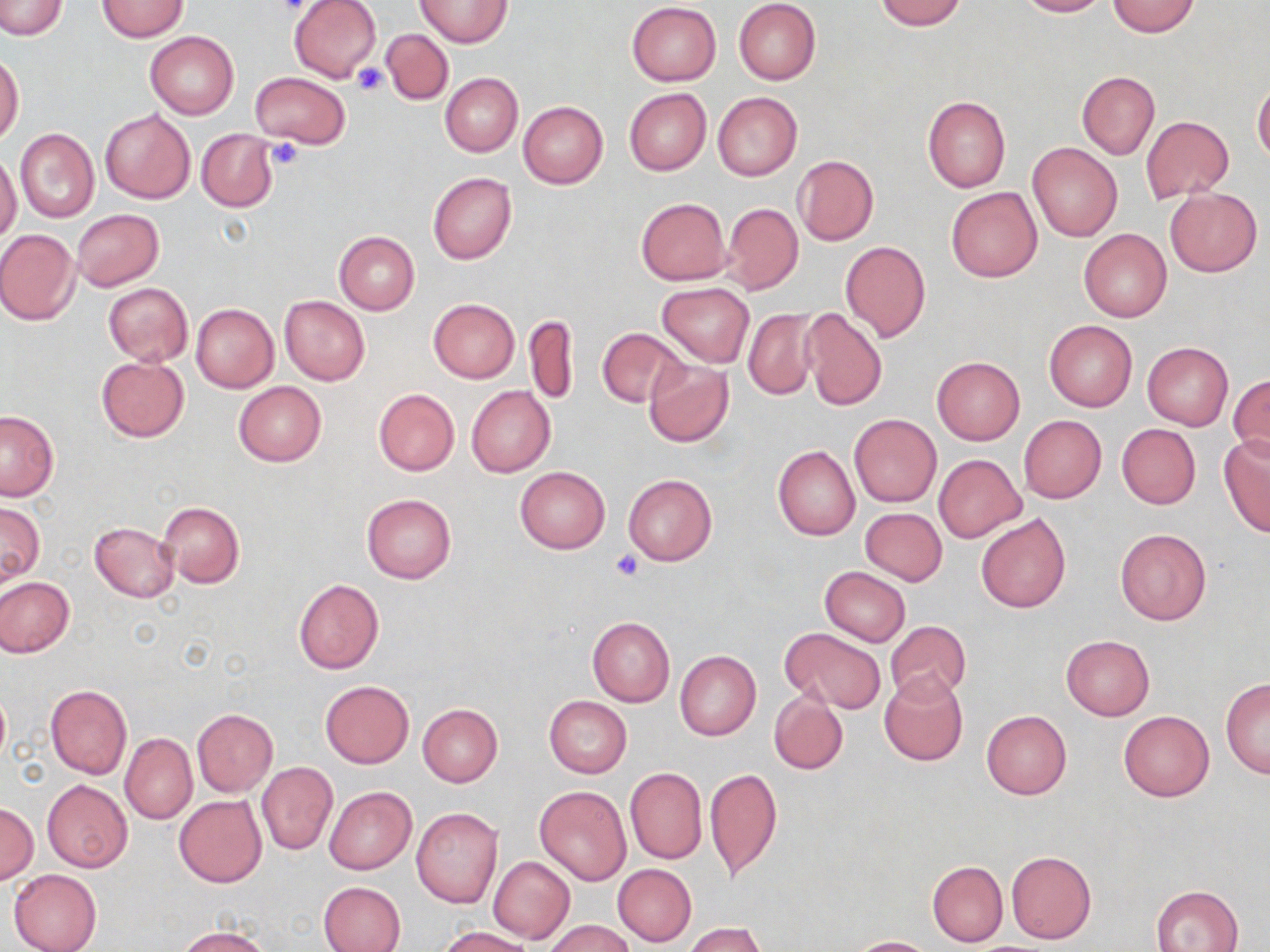

Approximate bounding boxes as named x1/y1/x2/y2 corners in pixels. Uninfected red blood cell locations: (x1=0, y1=0, x2=66, y2=40), (x1=289, y1=0, x2=380, y2=84), (x1=875, y1=0, x2=967, y2=30), (x1=1016, y1=0, x2=1110, y2=17), (x1=97, y1=1, x2=189, y2=41), (x1=415, y1=1, x2=510, y2=46), (x1=734, y1=1, x2=822, y2=85), (x1=626, y1=2, x2=721, y2=85), (x1=1107, y1=2, x2=1200, y2=37), (x1=382, y1=29, x2=453, y2=104), (x1=146, y1=31, x2=239, y2=119), (x1=0, y1=53, x2=24, y2=145), (x1=251, y1=71, x2=351, y2=150), (x1=1077, y1=71, x2=1159, y2=159), (x1=440, y1=73, x2=522, y2=157), (x1=1253, y1=79, x2=1270, y2=164), (x1=624, y1=87, x2=710, y2=176), (x1=712, y1=92, x2=802, y2=180), (x1=923, y1=96, x2=1011, y2=192), (x1=518, y1=100, x2=608, y2=189), (x1=100, y1=108, x2=195, y2=203), (x1=1141, y1=116, x2=1235, y2=202), (x1=196, y1=128, x2=277, y2=212), (x1=15, y1=129, x2=99, y2=223), (x1=1027, y1=142, x2=1123, y2=243), (x1=0, y1=154, x2=22, y2=245), (x1=792, y1=155, x2=879, y2=246), (x1=428, y1=172, x2=516, y2=265), (x1=945, y1=187, x2=1043, y2=282), (x1=1163, y1=187, x2=1262, y2=277), (x1=635, y1=197, x2=730, y2=285), (x1=723, y1=203, x2=802, y2=293), (x1=71, y1=209, x2=164, y2=291), (x1=1078, y1=228, x2=1171, y2=322), (x1=0, y1=229, x2=81, y2=325), (x1=334, y1=233, x2=419, y2=315), (x1=840, y1=241, x2=931, y2=341), (x1=656, y1=281, x2=755, y2=367), (x1=103, y1=283, x2=192, y2=365), (x1=279, y1=295, x2=370, y2=385), (x1=428, y1=299, x2=519, y2=383), (x1=191, y1=304, x2=279, y2=392), (x1=799, y1=306, x2=887, y2=411), (x1=741, y1=308, x2=818, y2=399), (x1=525, y1=314, x2=577, y2=406), (x1=1043, y1=320, x2=1137, y2=412), (x1=597, y1=328, x2=690, y2=407), (x1=1142, y1=342, x2=1233, y2=429), (x1=97, y1=355, x2=189, y2=442), (x1=932, y1=357, x2=1024, y2=444), (x1=643, y1=359, x2=734, y2=447), (x1=1229, y1=374, x2=1269, y2=464), (x1=233, y1=381, x2=326, y2=467), (x1=466, y1=386, x2=554, y2=478), (x1=374, y1=389, x2=459, y2=475), (x1=0, y1=410, x2=59, y2=501), (x1=848, y1=415, x2=941, y2=507), (x1=1018, y1=415, x2=1107, y2=503), (x1=1116, y1=423, x2=1201, y2=509), (x1=1219, y1=434, x2=1270, y2=536), (x1=773, y1=445, x2=860, y2=541), (x1=934, y1=454, x2=1024, y2=541), (x1=514, y1=466, x2=610, y2=555), (x1=624, y1=474, x2=717, y2=565), (x1=361, y1=493, x2=456, y2=582), (x1=0, y1=501, x2=44, y2=586), (x1=156, y1=501, x2=245, y2=588), (x1=859, y1=506, x2=947, y2=585), (x1=975, y1=512, x2=1071, y2=614), (x1=90, y1=521, x2=179, y2=602), (x1=1115, y1=527, x2=1212, y2=626), (x1=819, y1=566, x2=911, y2=647), (x1=0, y1=577, x2=74, y2=656), (x1=293, y1=579, x2=384, y2=675), (x1=586, y1=617, x2=675, y2=706), (x1=883, y1=623, x2=971, y2=705), (x1=781, y1=627, x2=886, y2=715), (x1=1061, y1=635, x2=1154, y2=719), (x1=675, y1=650, x2=761, y2=740), (x1=879, y1=670, x2=968, y2=767), (x1=1221, y1=677, x2=1270, y2=779), (x1=320, y1=681, x2=414, y2=768), (x1=45, y1=685, x2=132, y2=779), (x1=769, y1=692, x2=848, y2=774), (x1=544, y1=695, x2=632, y2=777), (x1=418, y1=703, x2=503, y2=786), (x1=192, y1=709, x2=277, y2=796), (x1=981, y1=710, x2=1072, y2=799), (x1=1117, y1=710, x2=1215, y2=802), (x1=121, y1=734, x2=196, y2=824), (x1=256, y1=762, x2=337, y2=855), (x1=624, y1=767, x2=707, y2=864), (x1=705, y1=767, x2=782, y2=881), (x1=42, y1=780, x2=133, y2=873), (x1=534, y1=785, x2=631, y2=886), (x1=325, y1=786, x2=416, y2=874), (x1=175, y1=796, x2=266, y2=887), (x1=0, y1=804, x2=39, y2=885), (x1=411, y1=807, x2=502, y2=907), (x1=1006, y1=851, x2=1097, y2=945), (x1=488, y1=856, x2=575, y2=944), (x1=927, y1=860, x2=1008, y2=947), (x1=613, y1=864, x2=697, y2=946), (x1=8, y1=868, x2=101, y2=952), (x1=319, y1=880, x2=406, y2=952), (x1=1152, y1=885, x2=1243, y2=951), (x1=546, y1=919, x2=633, y2=952), (x1=684, y1=923, x2=768, y2=952), (x1=437, y1=927, x2=535, y2=952), (x1=178, y1=928, x2=270, y2=952), (x1=846, y1=937, x2=940, y2=952). Platelet locations: (x1=352, y1=62, x2=387, y2=96), (x1=265, y1=139, x2=304, y2=171), (x1=610, y1=550, x2=644, y2=581). Slide-level diagnosis: no evidence of blood parasites. Image is 1270×952 pixels. Thin blood smear. May-Grünwald-Giemsa-stained preparation. One field of a larger specimen. Light microscopy. 1000x magnification.